Identify the blood parasite species.
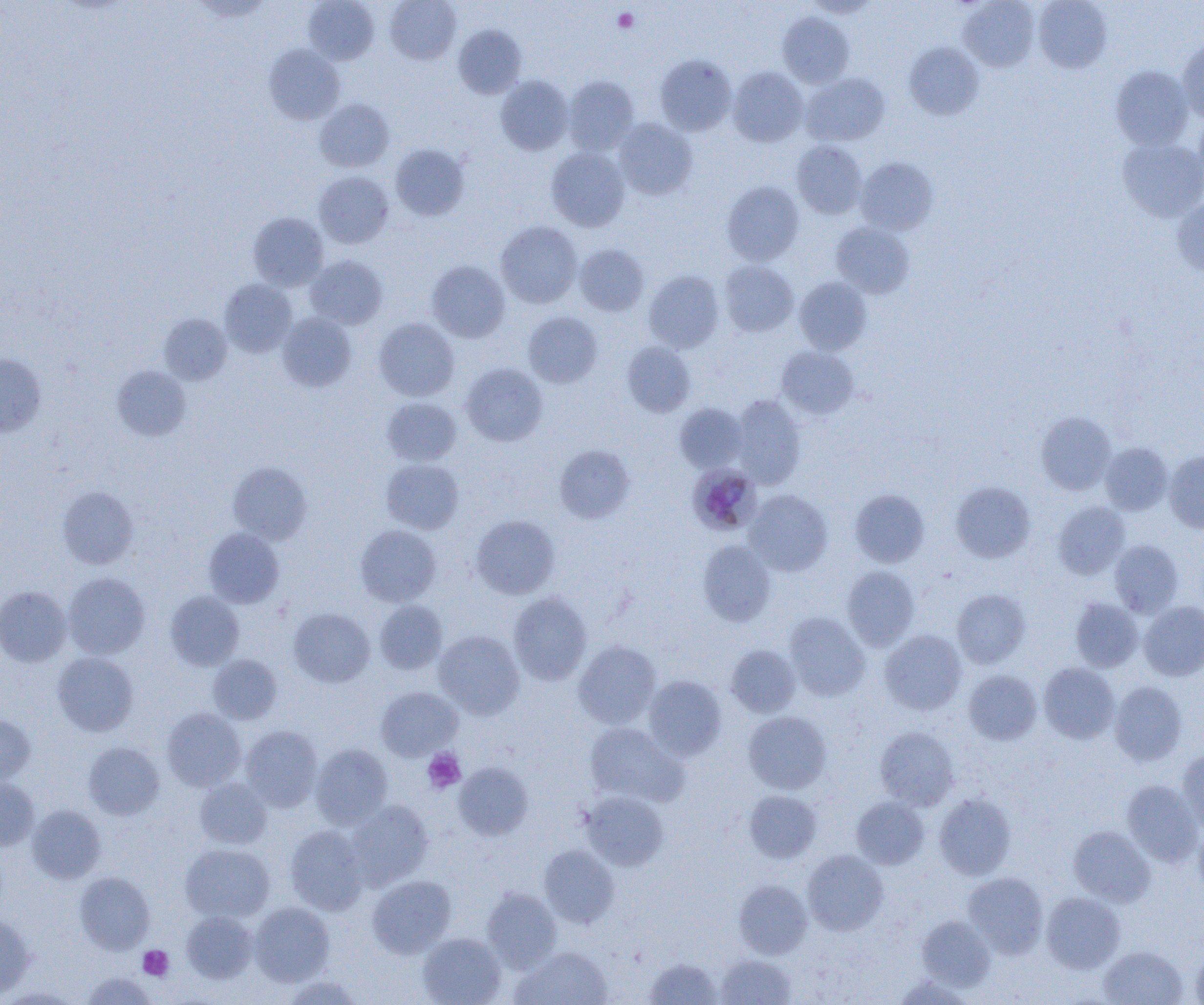

Plasmodium malariae.

platelet locations = approximate bounding boxes as [x1, y1, x2, y2] in pixels: [613, 8, 638, 32], [422, 748, 466, 794], [138, 945, 174, 980]
Plasmodium malariae-infected red blood cell locations = approximate bounding boxes as [x1, y1, x2, y2] in pixels: [688, 463, 760, 534]
magnification = 1000x
modality = optical microscopy
preparation = thin blood film
field of view = single
uninfected red blood cell locations = approximate bounding boxes as [x1, y1, x2, y2] in pixels: [303, 0, 379, 65], [385, 0, 461, 64], [804, 0, 880, 18], [959, 0, 1039, 71], [1034, 0, 1112, 73], [778, 12, 854, 88], [454, 24, 526, 98], [1177, 37, 1204, 122], [904, 43, 984, 119], [264, 44, 345, 124], [655, 54, 737, 135], [1110, 65, 1193, 150], [727, 67, 808, 146], [801, 73, 890, 146], [495, 75, 574, 155], [563, 75, 639, 155], [315, 98, 395, 172], [1193, 111, 1204, 192], [614, 118, 698, 200], [1117, 137, 1204, 222], [791, 140, 867, 219], [390, 143, 470, 221], [546, 147, 630, 231], [856, 157, 938, 235], [314, 171, 393, 248], [722, 181, 804, 265], [1172, 198, 1204, 277], [248, 212, 328, 291], [496, 221, 582, 308], [831, 222, 914, 298], [574, 244, 649, 316], [305, 255, 387, 329], [426, 260, 510, 343], [719, 260, 798, 337], [643, 270, 724, 353], [794, 277, 872, 355], [219, 279, 297, 357], [523, 311, 602, 388], [277, 312, 357, 392], [159, 314, 232, 385], [374, 317, 459, 401], [622, 341, 696, 417], [776, 346, 859, 419], [0, 354, 47, 436], [460, 363, 548, 446], [112, 365, 191, 441], [731, 394, 806, 488], [382, 397, 462, 466], [674, 403, 748, 473], [1035, 411, 1117, 495], [1100, 443, 1172, 515], [554, 444, 636, 523], [1164, 451, 1204, 533], [381, 458, 464, 534], [228, 462, 312, 545], [950, 481, 1035, 563], [57, 486, 139, 569], [744, 489, 833, 576], [849, 489, 930, 567], [1053, 501, 1130, 579], [470, 514, 560, 599], [355, 525, 441, 606], [203, 528, 285, 608], [697, 540, 776, 627], [1109, 540, 1184, 617], [842, 566, 921, 651], [63, 573, 150, 659], [0, 586, 71, 666], [952, 588, 1030, 668], [165, 591, 244, 670], [508, 592, 592, 685], [1070, 597, 1143, 672], [375, 600, 447, 674], [1138, 601, 1204, 681], [288, 608, 374, 687], [784, 612, 870, 700], [433, 630, 524, 719], [880, 630, 966, 715], [574, 640, 661, 728], [725, 644, 801, 718], [52, 652, 139, 736], [208, 654, 282, 724], [1039, 663, 1119, 744], [964, 669, 1042, 745], [644, 675, 727, 759], [1109, 681, 1188, 766], [376, 686, 462, 760], [162, 708, 246, 791], [743, 711, 832, 794], [0, 715, 35, 785], [584, 722, 687, 807], [241, 725, 322, 811], [875, 726, 959, 810], [83, 742, 164, 820], [310, 743, 393, 828], [1177, 749, 1204, 833], [454, 763, 533, 841], [194, 778, 272, 848], [0, 779, 39, 850], [1121, 780, 1202, 866], [744, 790, 822, 863], [581, 791, 668, 870], [934, 793, 1015, 880], [851, 796, 929, 869], [346, 800, 433, 890], [26, 805, 106, 883], [1193, 824, 1204, 899], [285, 825, 368, 915], [1068, 826, 1155, 907], [180, 843, 275, 923], [539, 844, 619, 928], [802, 849, 889, 935], [75, 872, 155, 954], [963, 872, 1048, 958], [367, 875, 456, 958], [733, 880, 812, 958], [482, 888, 561, 972], [1041, 892, 1125, 973], [249, 902, 334, 986], [181, 910, 258, 984], [0, 913, 35, 998], [916, 914, 995, 992], [418, 932, 506, 1005], [1098, 945, 1187, 1005], [1191, 946, 1204, 1005], [511, 947, 611, 1005], [715, 954, 797, 1004], [644, 957, 723, 1004], [80, 972, 159, 1004], [892, 974, 975, 1005], [283, 975, 364, 1004], [1, 987, 82, 1003]
image size = 1204×1005 pixels